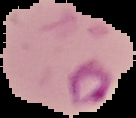
From a thin blood film. The area outside the segmented cell region is set to black. Malaria status: parasitized. Image is 136×118 pixels.